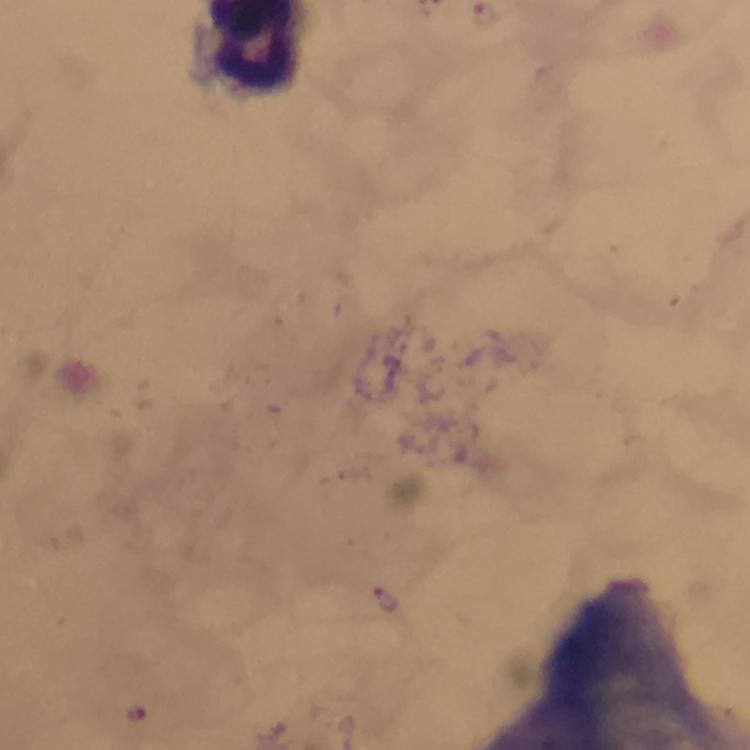
Approximate centers as {x, y} in pixels. Plasmodium parasite locations: {484, 15}, {388, 599}, {138, 714}. Giemsa stain. From a diagnostic examination for malaria. Thick blood film. Image is 750×750 pixels. Smartphone photograph taken through a microscope. 100x magnification. Cropped region of a single field of view. Immersion oil applied.